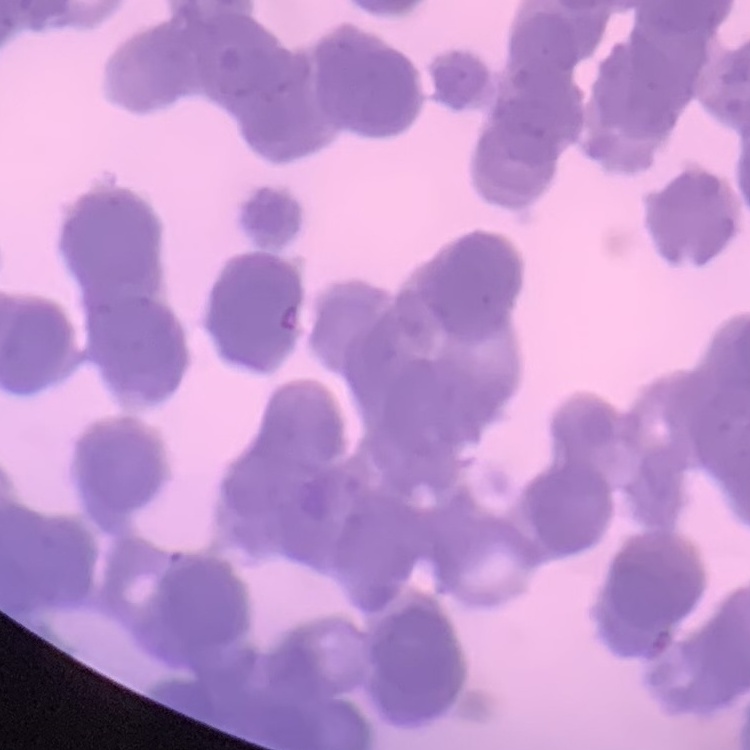 The red blood cells show rouleaux formation. Square crop of a larger photomicrograph. Thin blood smear. Field's or Giemsa stain.